Give the extent of all uninfected red blood cells.
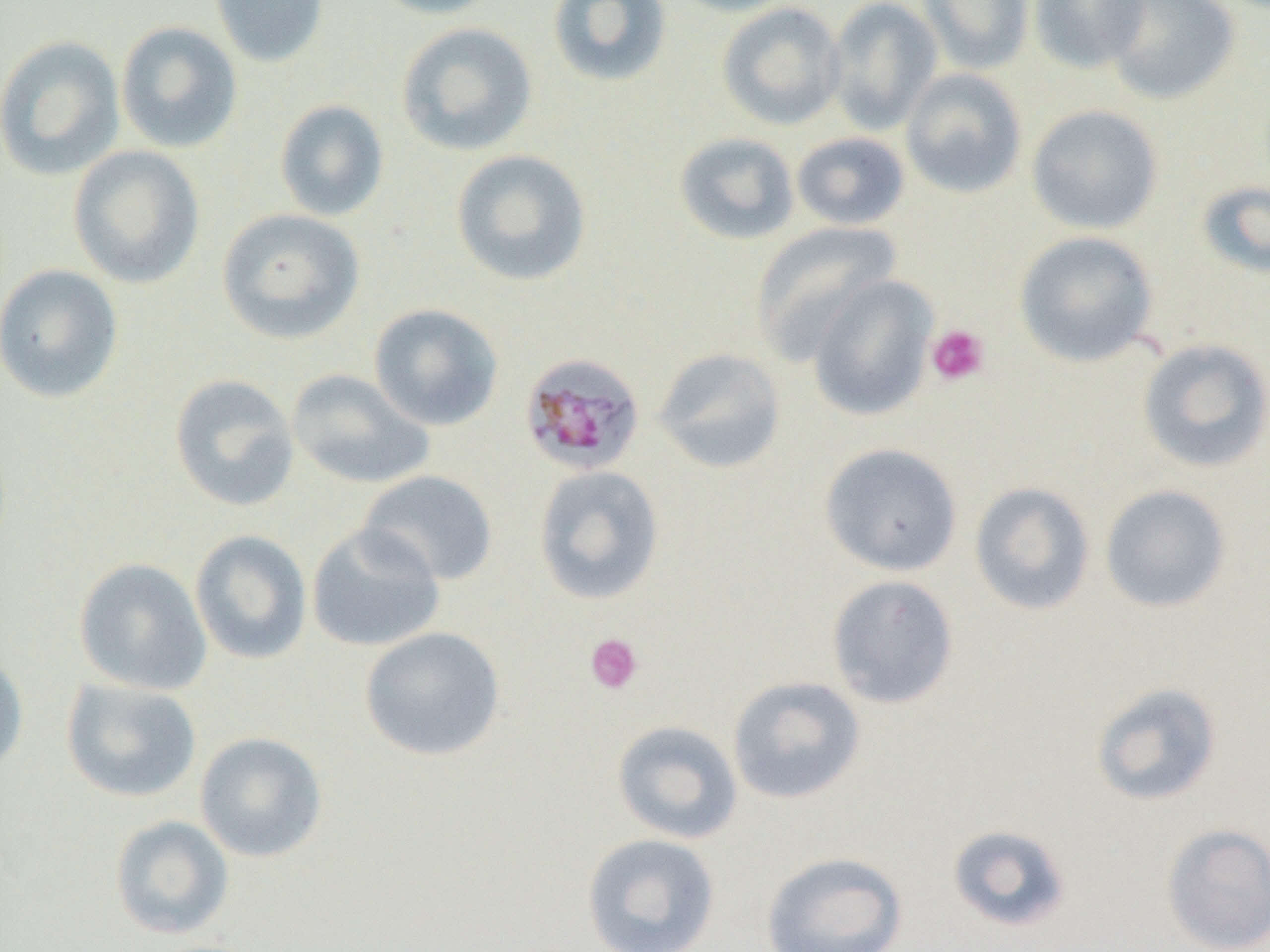
Approximate bounding boxes as (x1, y1, x2, y2) in pixels.
Uninfected red blood cells (subset): (210, 0, 329, 68), (366, 0, 506, 19), (664, 0, 802, 18), (824, 0, 943, 136), (918, 0, 1034, 75), (1028, 0, 1150, 73), (1102, 0, 1240, 106), (546, 1, 672, 88), (717, 2, 846, 131), (115, 21, 243, 154), (396, 22, 538, 157), (0, 34, 125, 181), (900, 68, 1027, 199), (275, 99, 389, 221), (1026, 104, 1163, 235), (791, 131, 910, 231), (673, 132, 800, 245), (68, 145, 206, 289), (450, 149, 592, 287), (1196, 180, 1270, 280), (217, 208, 365, 345), (749, 221, 902, 362), (1013, 231, 1159, 367), (0, 263, 124, 404), (368, 302, 504, 431), (1137, 338, 1270, 473), (652, 347, 786, 475), (286, 369, 434, 490), (169, 373, 300, 512), (819, 442, 963, 576), (533, 465, 665, 605), (358, 470, 499, 586), (969, 481, 1096, 616), (1099, 484, 1233, 613), (307, 523, 446, 652), (189, 529, 312, 665), (73, 557, 212, 696), (826, 574, 959, 709), (359, 626, 506, 761), (0, 652, 29, 779), (727, 676, 866, 805), (62, 678, 202, 803), (1090, 682, 1224, 806), (611, 720, 743, 844), (194, 731, 328, 862), (110, 815, 234, 939), (947, 823, 1072, 933), (1160, 823, 1270, 952), (581, 832, 721, 951), (760, 850, 907, 952).

Platelet locations (subset): (925, 324, 989, 386), (585, 633, 644, 695). Plasmodium malariae-infected red blood cell locations: (518, 352, 646, 476). Slide-level diagnosis: Plasmodium malariae. Image is 1270×952 pixels. Single field of view. 1000x magnification. Light microscopy. Thin blood smear.